Comment on the morphology of the erythrocytes.
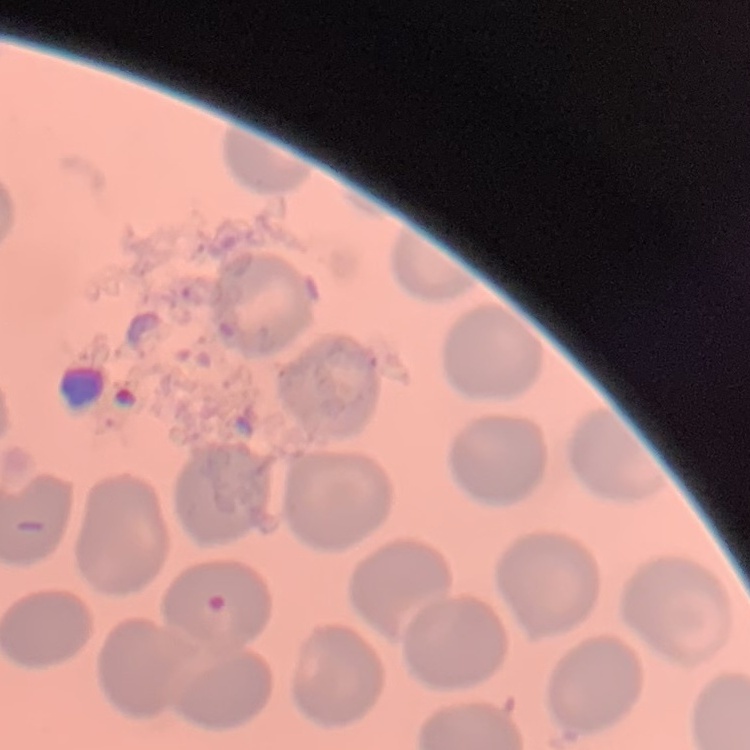

They show no rouleaux formation.

Summary:
  - Stain: Field's or Giemsa
  - Preparation: thin blood film
  - Image type: square crop of a larger photomicrograph